Assess this cell for malaria.
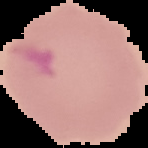

Parasitized.

Summary:
  - Image size: 148×148 pixels
  - Image type: cell region segmented out of the field of view; surrounding area masked to black
  - Preparation: thin blood smear